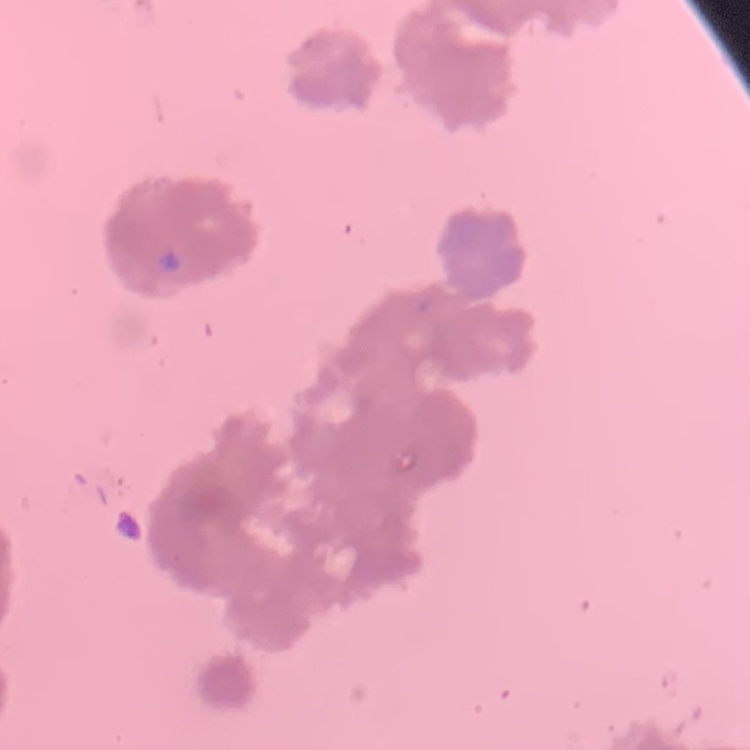
Summary:
  - Erythrocyte morphology: rouleaux formation
  - Stain: Field's or Giemsa
  - Image type: square crop of a larger photomicrograph
  - Preparation: thin peripheral smear